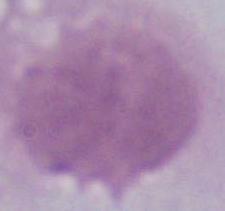
identification: erythrocyte
modality: photomicrograph
magnification: 1000x